Comment on the background quality.
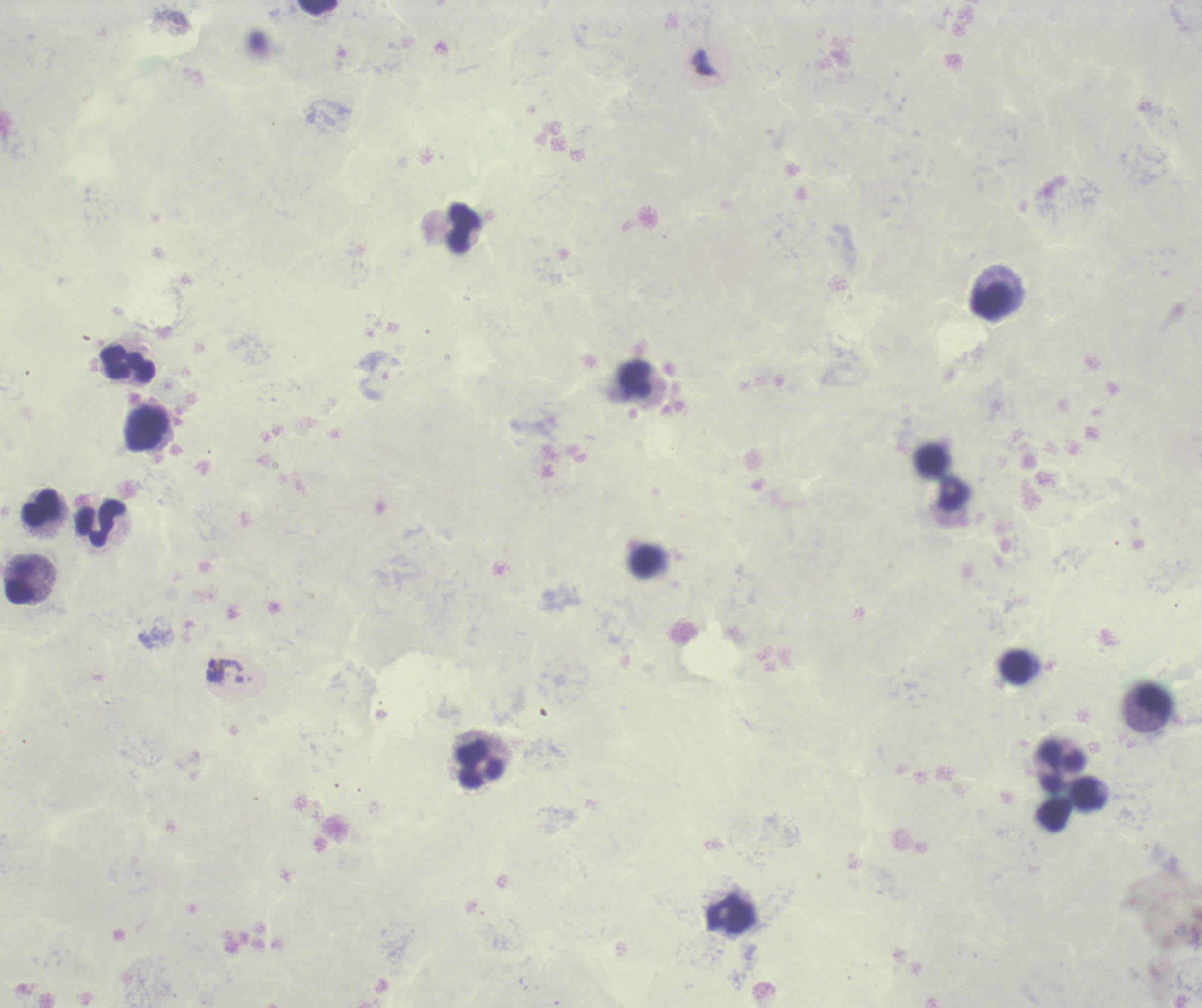
It is poor.

coordinate format = approximate centers as [x, y] in pixels
leukocyte locations = [318, 8], [465, 229], [992, 300], [128, 364], [635, 379], [147, 429], [41, 508], [100, 523], [21, 582], [1017, 667], [1153, 701], [480, 766], [1061, 766], [1088, 794], [732, 915]
trophozoite locations = [224, 670]
stain = Romanowsky
result = positive for Plasmodium parasites
magnification = 100x
context = previously used in an actual diagnosis
coloration quality = bad
image size = 1202×1008 pixels
preparation = thick smear of blood
field of view = one from this slide